Report the malaria status of this cell.
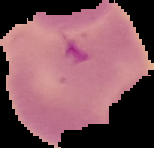

It is uninfected.

image type = segmented cell region with the area outside set to black
preparation = thin blood film
image size = 154×148 pixels